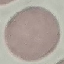
result = negative for malaria parasites
image type = cell patch, automatically extracted from a larger field of view and resized to 64 × 64 pixels
preparation = thin blood film
stain = Giemsa
capture = smartphone camera at the microscope eyepiece